Locate every blood parasite and identify its species.
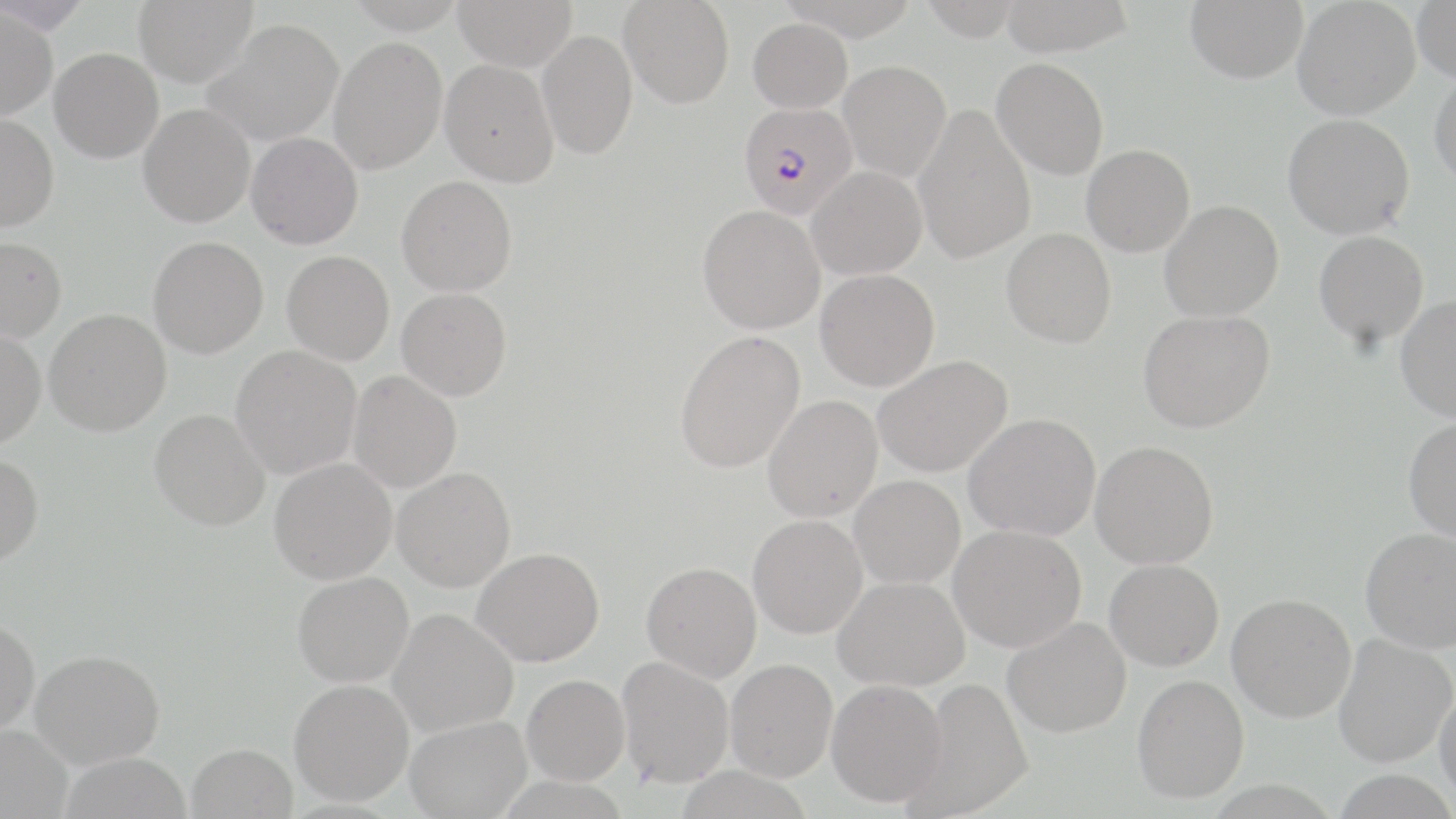
Approximate bounding boxes as named x1/y1/x2/y2 corners in pixels.
Plasmodium falciparum-infected red blood cells: (x1=739, y1=102, x2=857, y2=219).
No Plasmodium ovale, Plasmodium malariae, Plasmodium vivax, Babesia divergens, or Trypanosoma brucei observed.

slide_level_diagnosis: Plasmodium falciparum
image_size: 1456×819 pixels
uninfected_red_blood_cell_locations: 'approximate bounding boxes as named x1/y1/x2/y2 corners in pixels: (x1=133, y1=0, x2=258, y2=87), (x1=453, y1=0, x2=577, y2=71), (x1=999, y1=0, x2=1134, y2=56), (x1=1185, y1=0, x2=1308, y2=83), (x1=1292, y1=0, x2=1420, y2=120), (x1=619, y1=1, x2=735, y2=108), (x1=918, y1=1, x2=1024, y2=40), (x1=1412, y1=1, x2=1456, y2=84), (x1=0, y1=5, x2=58, y2=120), (x1=747, y1=17, x2=853, y2=113), (x1=202, y1=18, x2=344, y2=146), (x1=537, y1=30, x2=638, y2=160), (x1=329, y1=36, x2=447, y2=174), (x1=49, y1=47, x2=164, y2=163), (x1=991, y1=58, x2=1109, y2=179), (x1=439, y1=59, x2=559, y2=187), (x1=839, y1=60, x2=951, y2=181), (x1=1429, y1=69, x2=1456, y2=189), (x1=138, y1=103, x2=255, y2=228), (x1=913, y1=107, x2=1036, y2=264), (x1=0, y1=112, x2=59, y2=232), (x1=1282, y1=114, x2=1414, y2=239), (x1=245, y1=132, x2=363, y2=249), (x1=1082, y1=144, x2=1195, y2=257), (x1=807, y1=166, x2=927, y2=279), (x1=397, y1=175, x2=517, y2=296), (x1=1160, y1=200, x2=1283, y2=321), (x1=697, y1=204, x2=825, y2=334), (x1=1001, y1=228, x2=1116, y2=347), (x1=1314, y1=231, x2=1429, y2=348), (x1=0, y1=236, x2=66, y2=343), (x1=148, y1=236, x2=269, y2=358), (x1=282, y1=250, x2=395, y2=365), (x1=816, y1=269, x2=940, y2=391), (x1=397, y1=287, x2=512, y2=401), (x1=1395, y1=295, x2=1456, y2=421), (x1=44, y1=308, x2=171, y2=436), (x1=1138, y1=309, x2=1274, y2=432), (x1=0, y1=327, x2=46, y2=450), (x1=674, y1=330, x2=806, y2=473), (x1=230, y1=346, x2=362, y2=480), (x1=873, y1=355, x2=1012, y2=478), (x1=347, y1=370, x2=462, y2=493), (x1=763, y1=395, x2=883, y2=522), (x1=149, y1=408, x2=270, y2=530), (x1=963, y1=413, x2=1101, y2=541), (x1=1403, y1=418, x2=1456, y2=541), (x1=1091, y1=441, x2=1219, y2=569), (x1=0, y1=455, x2=44, y2=569), (x1=269, y1=458, x2=397, y2=584), (x1=392, y1=467, x2=516, y2=592), (x1=849, y1=475, x2=966, y2=588), (x1=748, y1=514, x2=868, y2=639), (x1=948, y1=524, x2=1086, y2=651), (x1=1361, y1=527, x2=1456, y2=652), (x1=472, y1=547, x2=604, y2=667), (x1=1104, y1=559, x2=1224, y2=671), (x1=642, y1=562, x2=762, y2=682), (x1=292, y1=571, x2=414, y2=687), (x1=833, y1=576, x2=970, y2=691), (x1=1227, y1=593, x2=1356, y2=722), (x1=388, y1=608, x2=518, y2=736), (x1=0, y1=617, x2=40, y2=736), (x1=1003, y1=617, x2=1131, y2=738), (x1=1334, y1=634, x2=1456, y2=766), (x1=30, y1=649, x2=165, y2=768), (x1=617, y1=656, x2=734, y2=788), (x1=725, y1=659, x2=838, y2=782), (x1=522, y1=674, x2=630, y2=785), (x1=1132, y1=674, x2=1249, y2=803), (x1=902, y1=677, x2=1034, y2=818), (x1=826, y1=678, x2=947, y2=808), (x1=289, y1=679, x2=415, y2=806), (x1=1435, y1=687, x2=1456, y2=803), (x1=405, y1=717, x2=531, y2=819), (x1=0, y1=724, x2=73, y2=819), (x1=187, y1=743, x2=298, y2=819), (x1=58, y1=752, x2=191, y2=819), (x1=675, y1=766, x2=814, y2=819)'
field_of_view: one of a larger specimen
preparation: thin blood smear
magnification: 1000x
stain: May-Grünwald-Giemsa
modality: optical microscopy